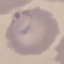 Result: malaria parasites detected. Thin blood smear. Acquired by smartphone through the microscope eyepiece. Automatically extracted cell patch, resized to 64 × 64 pixels. Giemsa stain.